Outline each blood parasite and name the species.
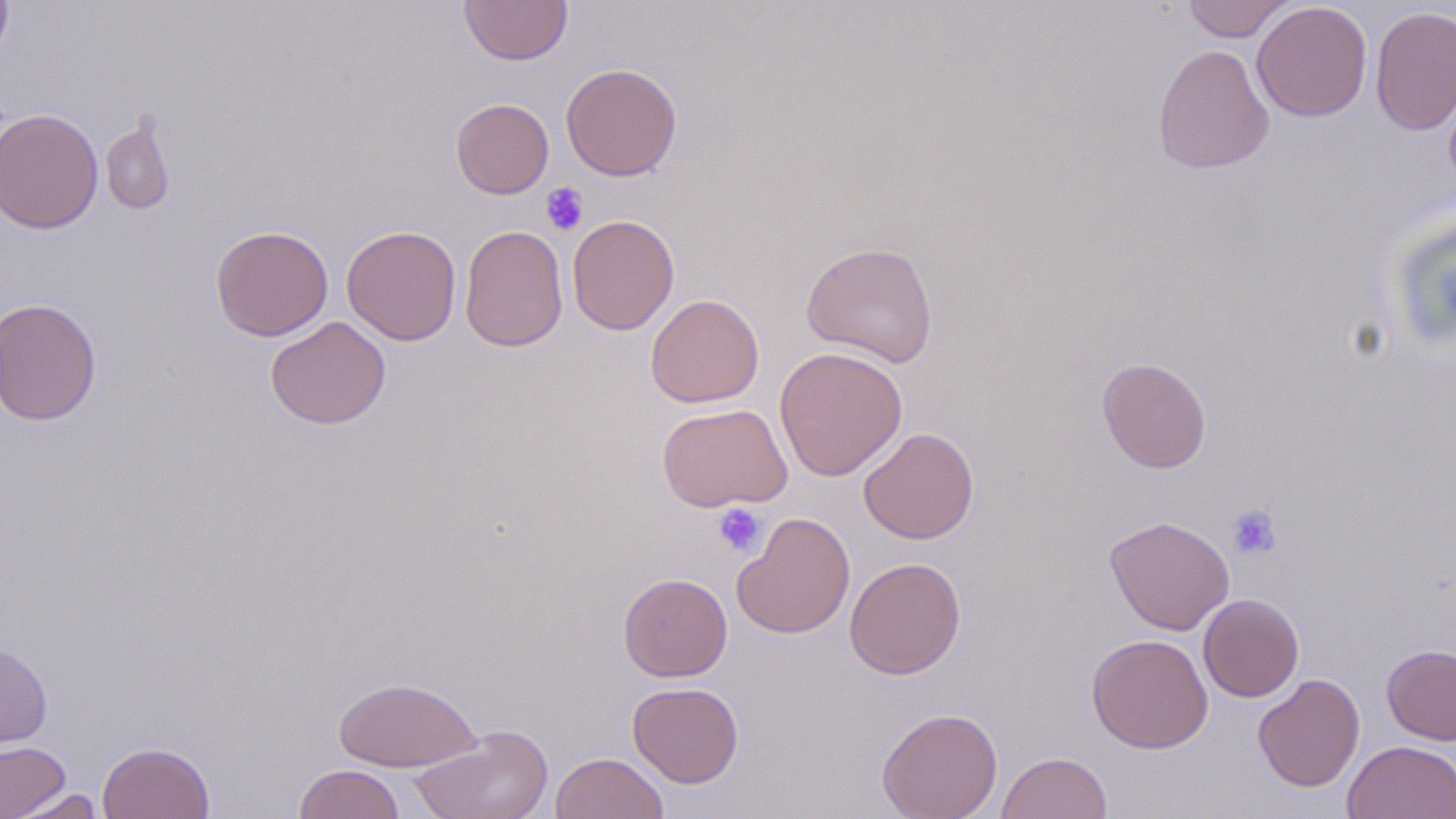
No blood parasites seen.

slide-level diagnosis = no evidence of blood parasites
field of view = one of a larger specimen
platelet locations = approximate bounding boxes as [x1, y1, x2, y2] in pixels: [540, 183, 590, 235], [712, 502, 767, 557], [1227, 504, 1283, 560]
image size = 1456×819 pixels
magnification = 1000x
uninfected red blood cell locations = approximate bounding boxes as [x1, y1, x2, y2] in pixels: [0, 0, 13, 67], [459, 0, 573, 66], [1182, 0, 1296, 42], [1252, 2, 1372, 122], [1370, 5, 1456, 137], [1152, 44, 1275, 174], [560, 63, 682, 181], [451, 98, 554, 199], [1, 109, 103, 234], [100, 111, 176, 216], [567, 214, 679, 335], [341, 224, 461, 345], [459, 224, 568, 352], [211, 225, 334, 341], [800, 242, 939, 367], [645, 293, 764, 408], [1, 297, 102, 426], [265, 316, 391, 429], [774, 346, 908, 481], [1097, 357, 1212, 473], [656, 403, 793, 512], [859, 427, 979, 544], [732, 512, 855, 639], [1104, 515, 1235, 635], [844, 557, 966, 679], [618, 572, 732, 681], [1198, 594, 1304, 702], [1086, 633, 1213, 754], [0, 640, 53, 749], [1381, 644, 1456, 745], [1253, 673, 1365, 792], [332, 676, 482, 773], [627, 681, 744, 787], [876, 707, 1004, 819], [409, 725, 555, 819], [0, 740, 71, 819], [1343, 740, 1456, 819], [97, 741, 215, 819], [996, 751, 1113, 819], [550, 752, 669, 818], [293, 764, 405, 819], [7, 788, 108, 818]
modality = light microscopy
stain = May-Grünwald-Giemsa
preparation = thin blood smear